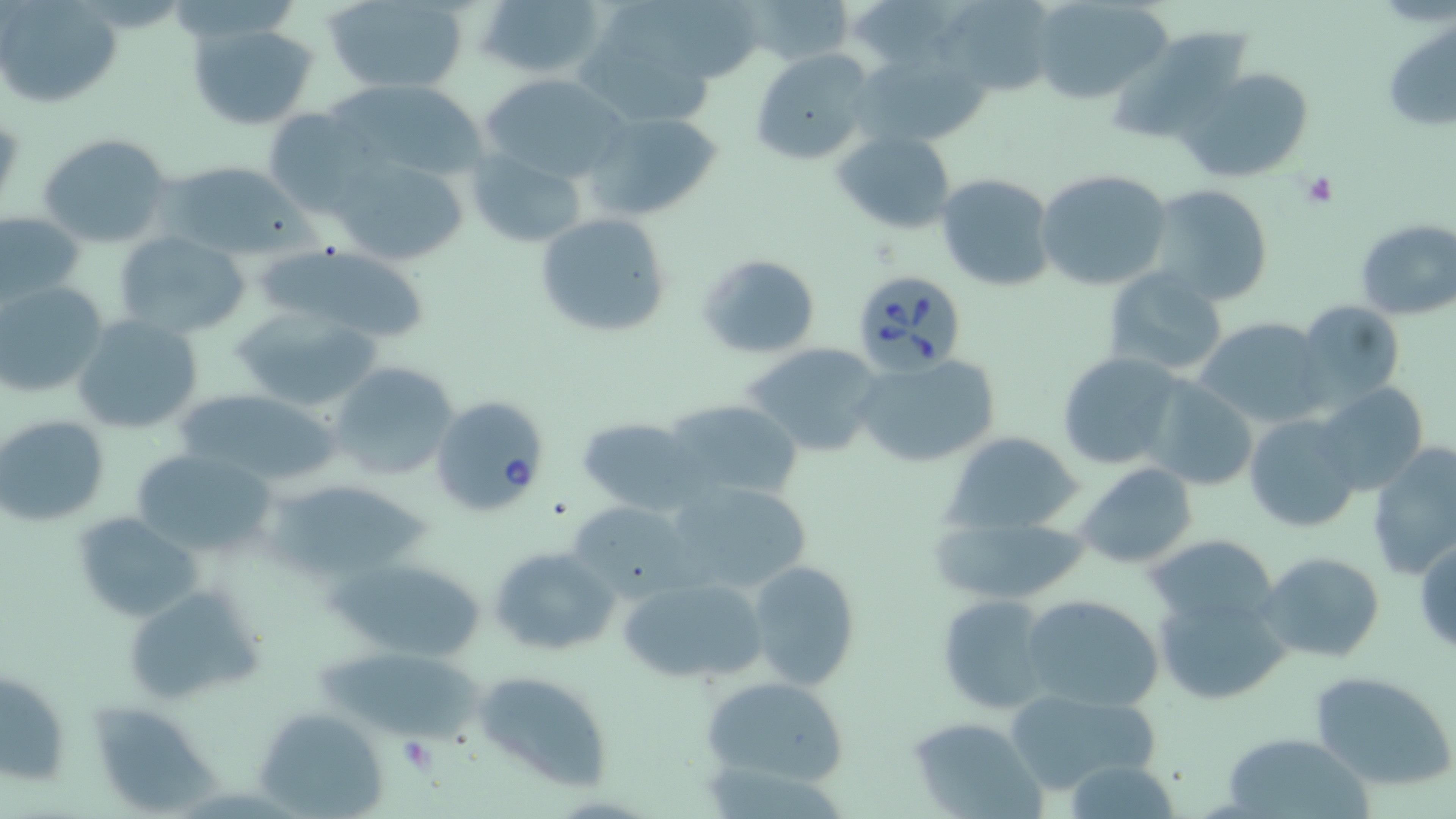

Approximate bounding boxes as [x1, y1, x2, y2] in pixels. Babesia divergens-infected red blood cell locations: [846, 267, 969, 378], [430, 394, 552, 520]. Uninfected red blood cell locations: [475, 0, 606, 83], [745, 0, 857, 65], [938, 0, 1057, 95], [1029, 0, 1173, 106], [323, 1, 469, 93], [0, 2, 120, 108], [573, 11, 728, 125], [1380, 15, 1455, 134], [186, 22, 319, 130], [1108, 27, 1258, 147], [856, 45, 992, 149], [751, 48, 877, 165], [1176, 66, 1316, 185], [479, 73, 633, 186], [260, 107, 376, 218], [584, 110, 725, 221], [833, 129, 957, 235], [38, 133, 175, 250], [321, 148, 473, 269], [466, 149, 587, 249], [160, 162, 307, 260], [1035, 167, 1173, 293], [935, 172, 1056, 292], [1146, 183, 1275, 307], [535, 212, 672, 340], [0, 213, 82, 310], [1354, 218, 1456, 320], [113, 231, 251, 340], [261, 247, 438, 346], [696, 252, 821, 358], [1103, 266, 1229, 379], [1, 282, 106, 399], [1290, 298, 1406, 415], [231, 308, 384, 412], [71, 313, 204, 436], [1193, 317, 1329, 428], [744, 344, 888, 457], [1057, 351, 1185, 471], [851, 354, 1001, 470], [327, 362, 458, 481], [1139, 379, 1259, 491], [1312, 382, 1429, 496], [173, 389, 344, 487], [662, 397, 806, 504], [1242, 414, 1360, 533], [0, 415, 110, 525], [577, 416, 702, 514], [944, 432, 1086, 535], [1366, 442, 1456, 582], [132, 448, 278, 560], [1075, 462, 1200, 570], [663, 477, 816, 597], [268, 478, 433, 583], [566, 501, 695, 599], [71, 512, 202, 623], [930, 515, 1091, 606], [1147, 530, 1281, 634], [1415, 537, 1456, 656], [489, 544, 620, 659], [1257, 552, 1386, 662], [332, 556, 488, 662], [746, 560, 862, 691], [619, 576, 768, 686], [123, 582, 266, 706], [1152, 587, 1288, 705], [1020, 594, 1166, 711], [934, 595, 1055, 713], [1, 666, 71, 786], [473, 669, 614, 791], [1307, 670, 1456, 790], [699, 674, 851, 788], [1004, 686, 1163, 798], [84, 702, 227, 812], [253, 708, 387, 818], [906, 714, 1044, 816], [1219, 731, 1373, 819]. Platelet locations: [1303, 171, 1338, 208], [393, 738, 438, 776]. Slide-level diagnosis: Babesia divergens. Optical microscopy. Image is 1456×819 pixels. Thin blood smear. May-Grünwald-Giemsa stain. Single field of view. Captured at 1000x magnification.